State which parasite is depicted.
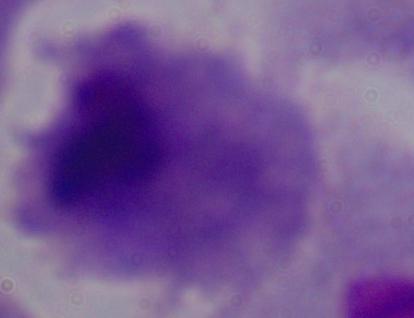
This is a trichomonad.

Summary:
  - Modality: photomicrograph
  - Magnification: 1000x